State the blood parasite species.
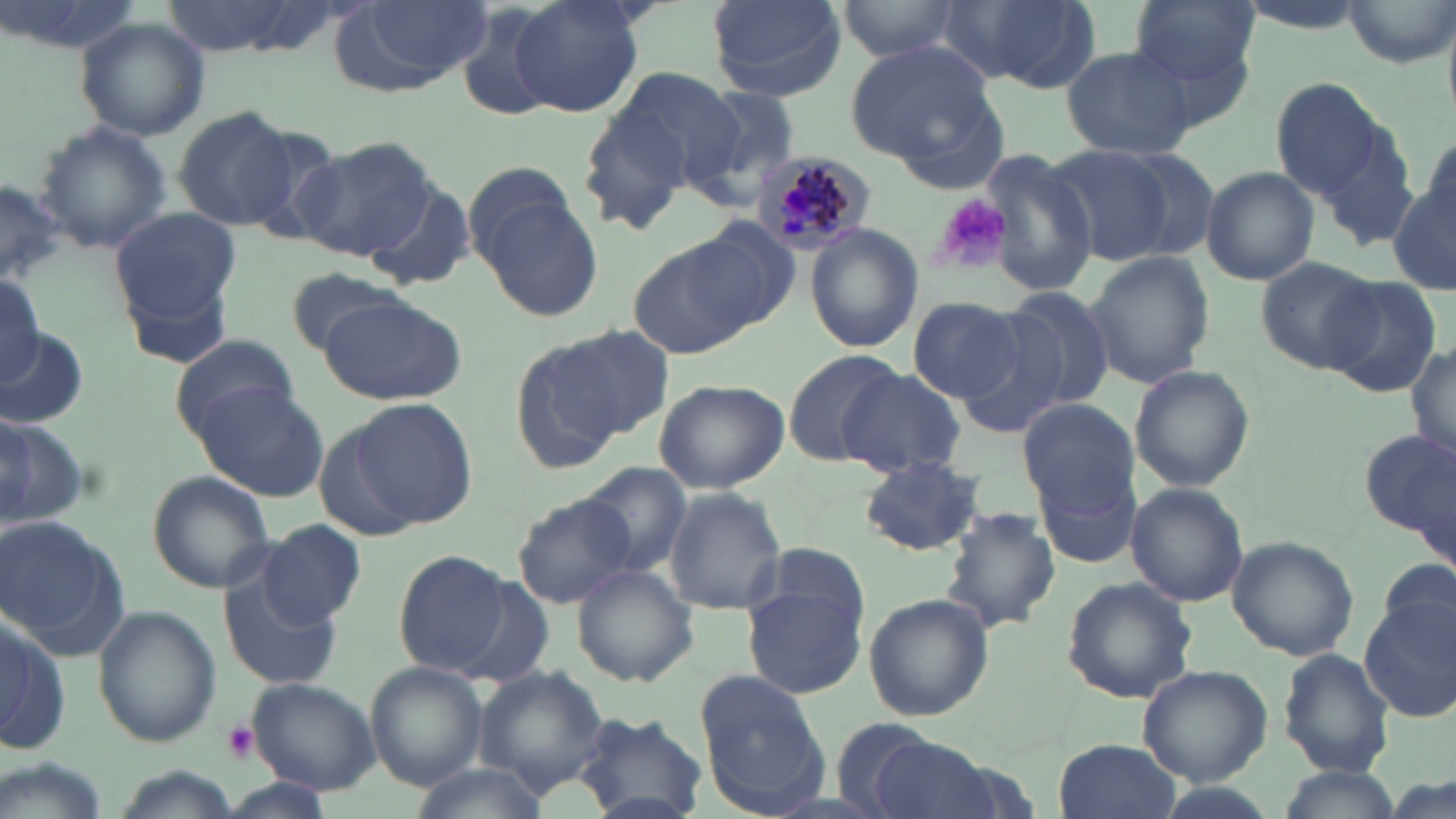
Plasmodium malariae.

{
  "uninfected_red_blood_cell_locations": "approximate bounding boxes as (x1, y1, x2, y2) in pixels: (337, 0, 490, 90), (509, 0, 645, 119), (705, 0, 846, 100), (831, 0, 971, 63), (955, 0, 1101, 94), (1128, 0, 1259, 104), (1340, 0, 1452, 69), (451, 5, 561, 123), (75, 15, 210, 142), (845, 39, 997, 168), (1061, 43, 1200, 162), (594, 65, 745, 205), (1268, 76, 1392, 204), (682, 86, 803, 202), (171, 107, 298, 229), (34, 121, 174, 253), (1416, 127, 1455, 235), (290, 138, 436, 262), (1044, 143, 1178, 266), (1105, 143, 1225, 264), (980, 153, 1099, 299), (461, 160, 579, 266), (1200, 167, 1319, 285), (1387, 179, 1456, 299), (0, 180, 64, 287), (362, 182, 476, 292), (475, 195, 606, 323), (111, 206, 240, 323), (690, 218, 803, 328), (804, 224, 920, 353), (631, 243, 755, 360), (1085, 249, 1214, 389), (1256, 256, 1384, 374), (282, 268, 410, 356), (0, 276, 48, 388), (1321, 276, 1443, 397), (995, 286, 1120, 410), (316, 293, 466, 404), (907, 295, 1029, 404), (954, 316, 1071, 442), (2, 323, 89, 431), (526, 326, 670, 458), (168, 334, 302, 439), (1409, 338, 1455, 468), (783, 349, 903, 466), (1127, 363, 1252, 493), (835, 370, 968, 479), (653, 379, 790, 494), (190, 382, 329, 503), (348, 398, 479, 529), (1019, 399, 1137, 512), (0, 408, 91, 530), (1357, 423, 1456, 562), (859, 456, 986, 555), (577, 462, 693, 577), (147, 470, 276, 593), (1037, 470, 1141, 569), (1125, 484, 1249, 607), (662, 486, 788, 615), (512, 494, 635, 609), (941, 510, 1061, 632), (0, 517, 129, 657), (257, 518, 366, 628), (1226, 537, 1359, 661), (753, 543, 871, 641), (392, 549, 518, 680), (572, 563, 699, 687), (220, 566, 344, 691), (1060, 577, 1199, 704), (450, 579, 555, 687), (741, 581, 868, 700), (863, 594, 992, 722), (1361, 600, 1456, 724), (92, 606, 220, 745), (0, 610, 71, 758), (1277, 649, 1395, 776), (365, 661, 485, 791), (471, 665, 611, 795), (1138, 665, 1272, 786), (694, 670, 830, 814), (248, 679, 379, 795), (574, 711, 707, 819), (827, 716, 948, 818), (870, 736, 1001, 819), (1053, 737, 1182, 819), (408, 764, 551, 819), (1273, 765, 1396, 819), (220, 780, 334, 816)",
  "preparation": "thin blood smear",
  "modality": "light microscopy",
  "stain": "May-Grünwald-Giemsa",
  "magnification": "1000x",
  "plasmodium_malariae_infected_red_blood_cell_locations": "approximate bounding boxes as (x1, y1, x2, y2) in pixels: (752, 150, 874, 255)",
  "platelet_locations": "approximate bounding boxes as (x1, y1, x2, y2) in pixels: (932, 194, 1012, 276), (221, 720, 259, 764)",
  "image_size": "1456×819 pixels",
  "field_of_view": "single"
}